Report the malaria status of this cell.
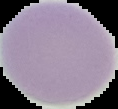
It is uninfected.

From a thin blood smear. Image is 118×109 pixels. The area outside the segmented cell region is set to black.